Assess this cell for malaria.
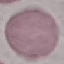

It is uninfected.

Automatically extracted cell patch, resized to 64 × 64 pixels. Thin smear of blood. Acquired by smartphone through the microscope eyepiece. Giemsa stain.